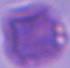

{
  "magnification": "1000x",
  "modality": "photomicrograph",
  "identification": "erythrocyte"
}